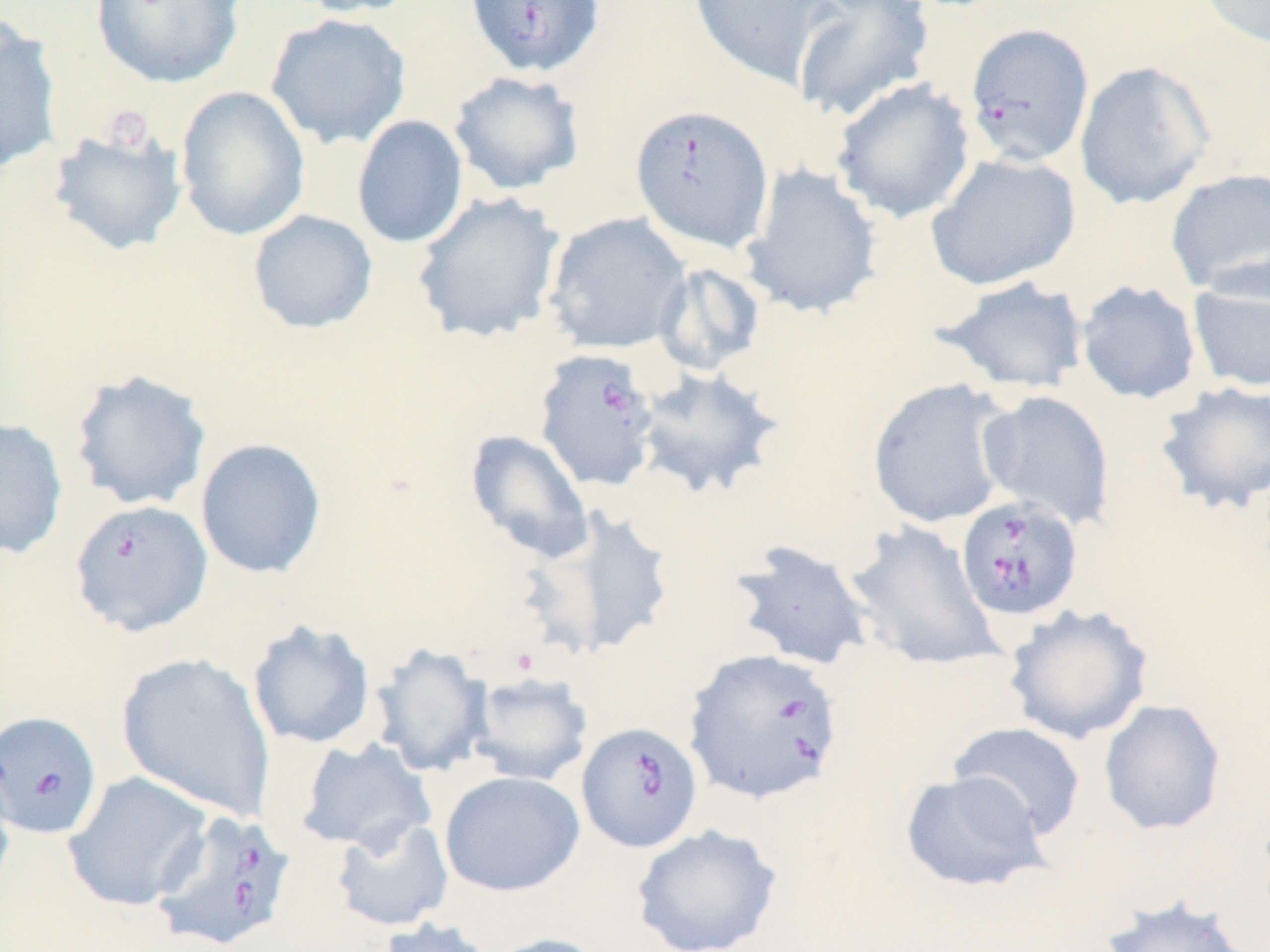
Summary:
  - Coordinate format: approximate bounding boxes as [x1, y1, x2, y2] in pixels
  - Babesia divergens-infected red blood cell locations: [464, 0, 605, 79], [964, 22, 1094, 168], [630, 104, 775, 252], [534, 349, 660, 491], [954, 495, 1084, 623], [68, 498, 213, 637], [683, 648, 845, 805], [0, 710, 102, 839], [577, 722, 703, 852], [149, 809, 296, 952]
  - Uninfected red blood cell locations: [90, 0, 245, 88], [291, 0, 421, 19], [689, 0, 839, 89], [790, 0, 936, 123], [1197, 0, 1270, 49], [265, 13, 411, 150], [0, 18, 64, 176], [1074, 61, 1215, 210], [448, 70, 585, 196], [832, 78, 976, 224], [175, 86, 310, 241], [351, 114, 468, 249], [47, 125, 188, 257], [924, 152, 1082, 291], [740, 162, 884, 320], [1165, 168, 1270, 298], [411, 191, 565, 344], [247, 209, 378, 334], [543, 212, 692, 355], [654, 262, 766, 377], [1187, 266, 1270, 394], [935, 276, 1090, 396], [1075, 280, 1202, 405], [634, 366, 784, 500], [69, 368, 212, 512], [867, 377, 1016, 529], [1153, 380, 1270, 515], [977, 390, 1116, 531], [0, 417, 69, 560], [465, 429, 595, 564], [195, 438, 327, 579], [530, 505, 680, 659], [844, 521, 1002, 673], [727, 540, 875, 672], [1003, 604, 1154, 745], [246, 619, 377, 749], [369, 643, 494, 778], [116, 652, 277, 821], [467, 672, 594, 787], [1099, 699, 1227, 835], [947, 722, 1087, 840], [295, 737, 437, 855], [0, 760, 17, 908], [900, 770, 1051, 892], [63, 771, 213, 912], [439, 771, 585, 897], [330, 816, 455, 931], [631, 824, 783, 952], [1099, 895, 1254, 952], [376, 918, 498, 952], [484, 933, 613, 952]
  - Slide-level diagnosis: Babesia divergens
  - Preparation: thin blood film
  - Field of view: one of a larger specimen
  - Modality: optical microscopy
  - Magnification: 1000x
  - Stain: May-Grünwald-Giemsa
  - Image size: 1270×952 pixels